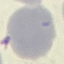

{
  "result": "negative for malaria parasites",
  "stain": "Giemsa",
  "preparation": "thin smear",
  "capture": "smartphone through the microscope eyepiece",
  "image_type": "automatically extracted cell patch, resized to 64 × 64 pixels"
}